Assess for Plasmodium parasites.
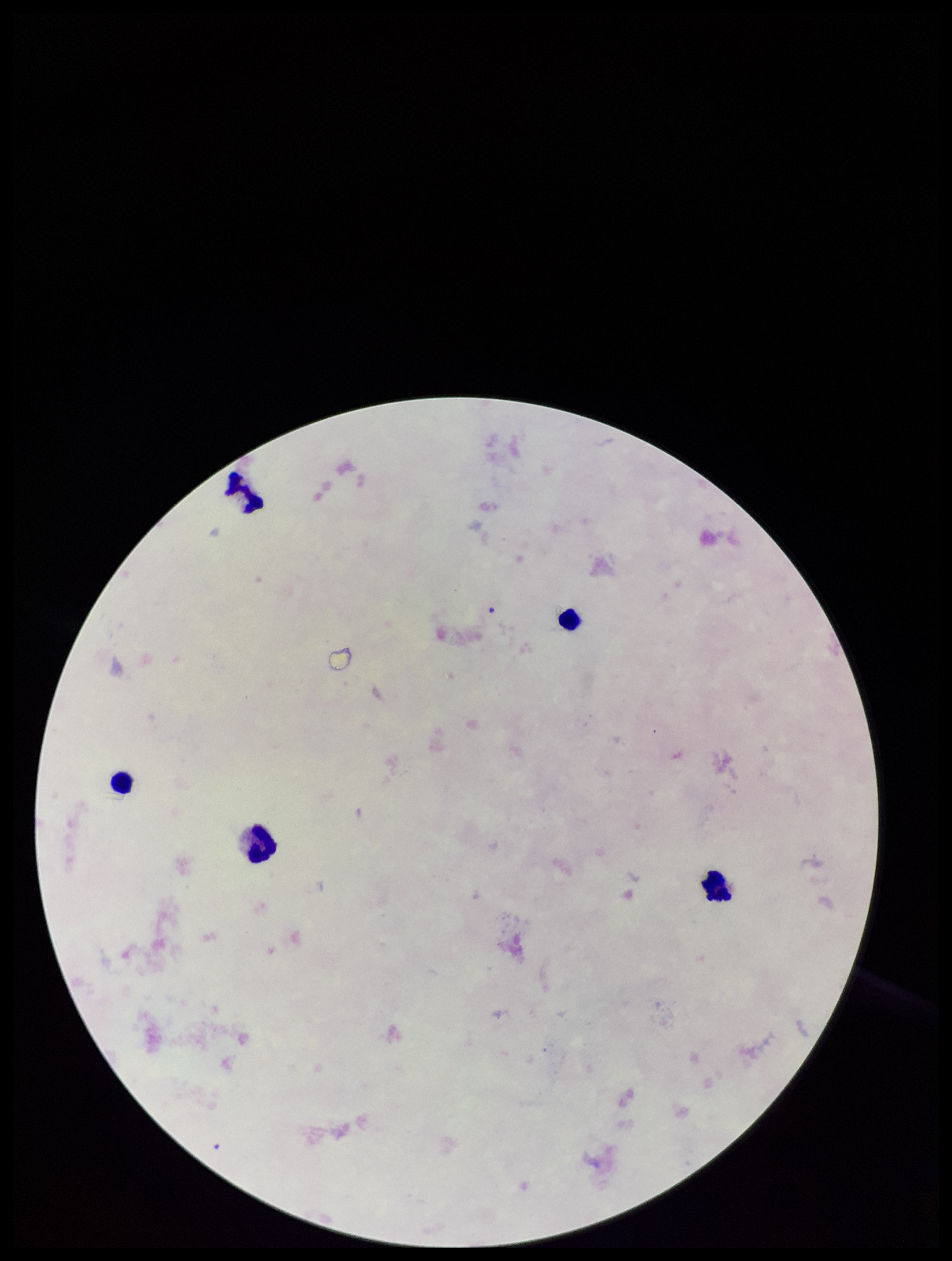
None seen.

field of view = one from this slide
leukocyte count = 5
patient malaria status = infected
preparation = thick smear
image size = 952×1261 pixels
parasite count = 0
species reported for this patient = Plasmodium falciparum
capture = smartphone photograph through the microscope eyepiece
stain = Giemsa